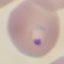
Malaria status: parasitized. Thin blood smear. Automatically extracted cell patch, resized to 64 × 64 pixels. Giemsa-stained preparation. Photographed with a smartphone camera at the microscope eyepiece.